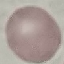

Summary:
  - Malaria status: uninfected
  - Stain: Giemsa
  - Preparation: thin blood film
  - Image type: cell patch, automatically extracted from a larger field of view and resized to 64 × 64 pixels
  - Capture: smartphone through the microscope eyepiece